Report the malaria status of this cell.
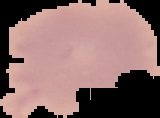
Uninfected.

preparation = thin blood smear
image type = cell region segmented out of the field of view; surrounding area masked to black
image size = 160×118 pixels